Assess the morphology of the red blood cells.
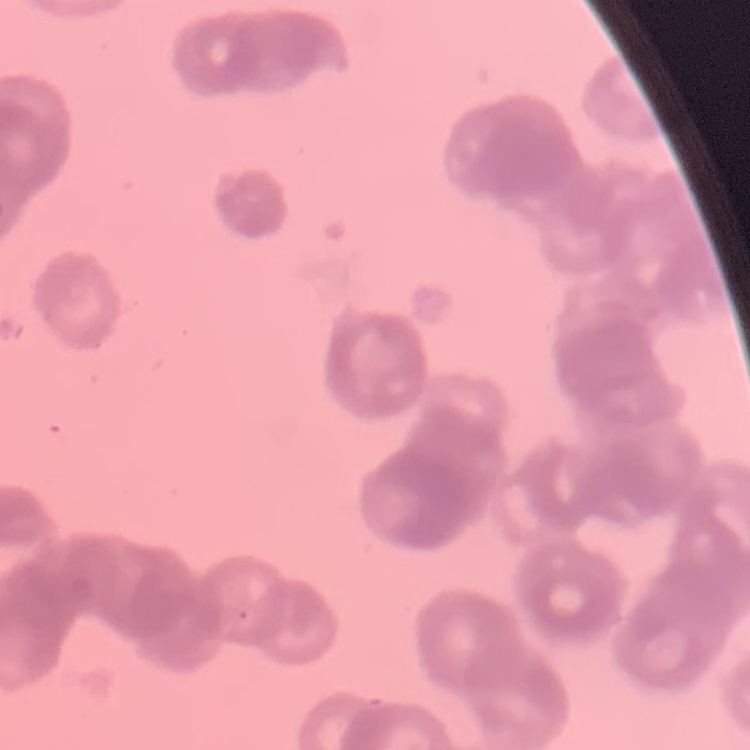

They show rouleaux formation.

image type = square crop of a larger photomicrograph
preparation = thin peripheral smear
stain = Field's or Giemsa